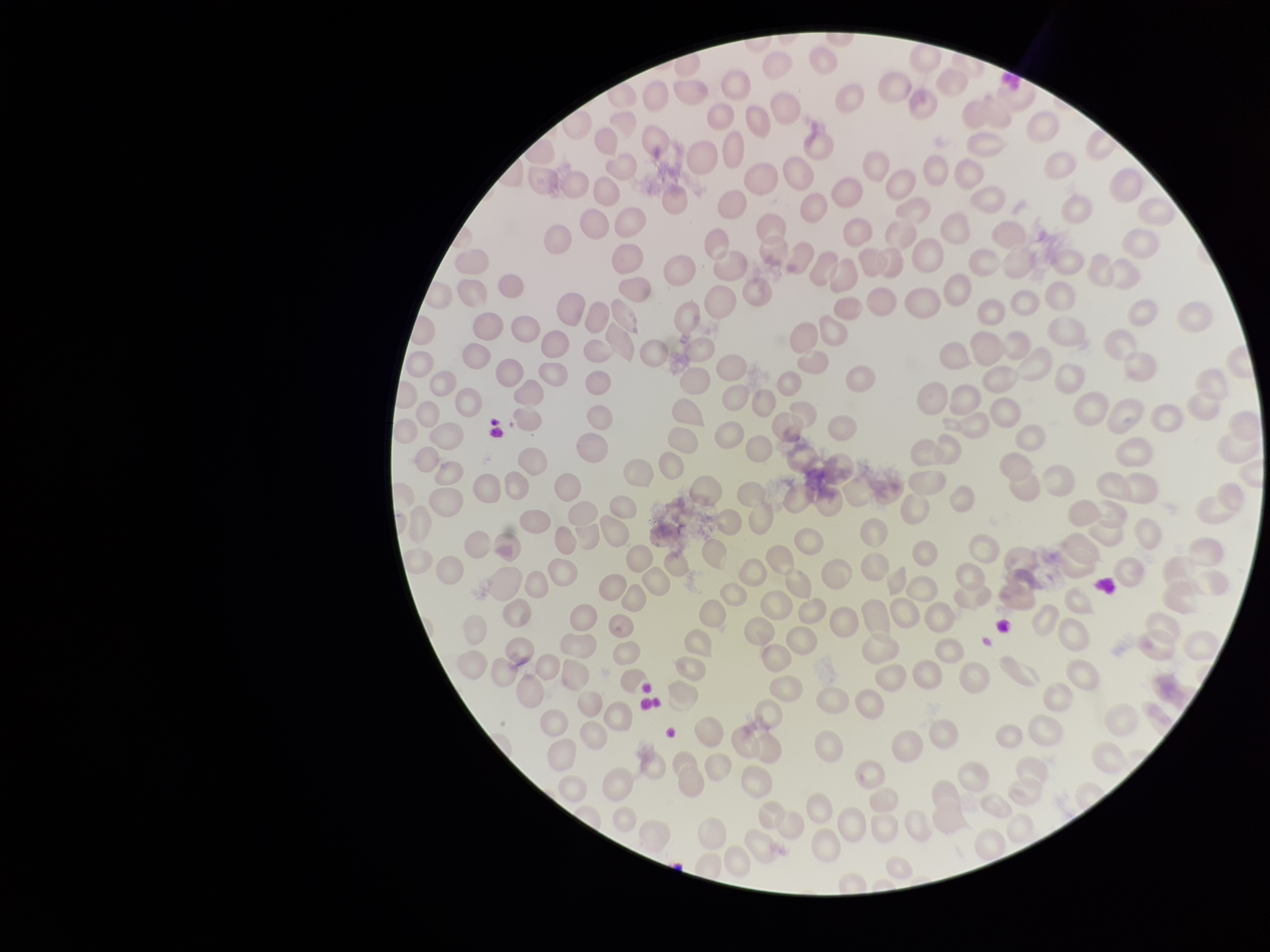
image size = 1270×952 pixels
parasitized red blood cells = none seen
patient malaria status = negative
parasitized red blood cell count = 0
field of view = one from this slide
red blood cell count = 231
capture = smartphone photograph through the microscope eyepiece
stain = Giemsa
preparation = thin blood smear